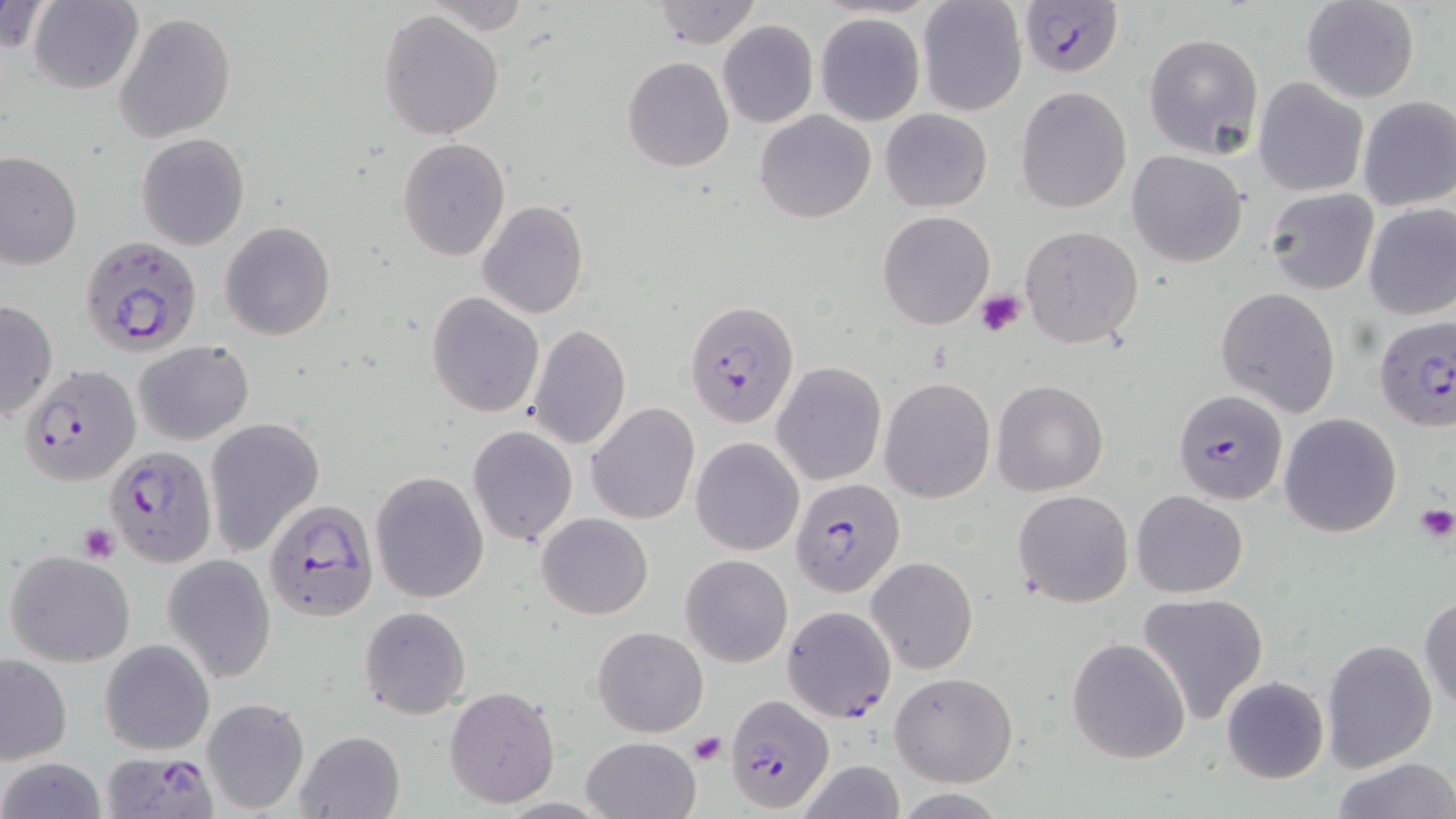
{
  "slide_level_diagnosis": "Plasmodium falciparum",
  "uninfected_red_blood_cell_locations": "approximate bounding boxes as named x1/y1/x2/y2 corners in pixels: (x1=0, y1=0, x2=54, y2=54), (x1=26, y1=0, x2=145, y2=93), (x1=650, y1=0, x2=760, y2=48), (x1=1299, y1=0, x2=1419, y2=102), (x1=916, y1=1, x2=1028, y2=116), (x1=378, y1=9, x2=505, y2=141), (x1=815, y1=11, x2=925, y2=125), (x1=114, y1=12, x2=236, y2=143), (x1=717, y1=20, x2=818, y2=128), (x1=1142, y1=32, x2=1265, y2=159), (x1=622, y1=56, x2=734, y2=172), (x1=1254, y1=78, x2=1369, y2=197), (x1=1015, y1=87, x2=1132, y2=214), (x1=1356, y1=97, x2=1456, y2=211), (x1=880, y1=108, x2=992, y2=212), (x1=755, y1=109, x2=875, y2=223), (x1=136, y1=133, x2=250, y2=250), (x1=397, y1=138, x2=510, y2=261), (x1=1126, y1=150, x2=1250, y2=267), (x1=0, y1=151, x2=82, y2=269), (x1=1263, y1=189, x2=1379, y2=294), (x1=479, y1=201, x2=589, y2=319), (x1=1361, y1=203, x2=1456, y2=321), (x1=877, y1=210, x2=994, y2=330), (x1=220, y1=221, x2=336, y2=341), (x1=1020, y1=226, x2=1142, y2=347), (x1=1216, y1=287, x2=1342, y2=416), (x1=426, y1=292, x2=543, y2=416), (x1=1, y1=299, x2=57, y2=422), (x1=527, y1=324, x2=632, y2=451), (x1=133, y1=340, x2=255, y2=445), (x1=772, y1=363, x2=886, y2=484), (x1=880, y1=377, x2=996, y2=503), (x1=991, y1=379, x2=1108, y2=495), (x1=587, y1=403, x2=700, y2=524), (x1=1278, y1=413, x2=1402, y2=537), (x1=204, y1=417, x2=324, y2=556), (x1=467, y1=425, x2=577, y2=547), (x1=691, y1=437, x2=804, y2=556), (x1=370, y1=471, x2=490, y2=603), (x1=1012, y1=490, x2=1134, y2=608), (x1=1131, y1=490, x2=1248, y2=598), (x1=536, y1=512, x2=654, y2=619), (x1=2, y1=552, x2=134, y2=666), (x1=162, y1=553, x2=277, y2=684), (x1=679, y1=553, x2=794, y2=668), (x1=866, y1=557, x2=977, y2=675), (x1=1136, y1=592, x2=1270, y2=726), (x1=1419, y1=592, x2=1456, y2=716), (x1=359, y1=606, x2=470, y2=719), (x1=592, y1=625, x2=709, y2=737), (x1=1067, y1=637, x2=1191, y2=765), (x1=100, y1=638, x2=215, y2=755), (x1=1320, y1=638, x2=1437, y2=773), (x1=0, y1=654, x2=73, y2=764), (x1=890, y1=672, x2=1018, y2=788), (x1=1222, y1=676, x2=1329, y2=784), (x1=445, y1=687, x2=560, y2=808), (x1=201, y1=697, x2=310, y2=813), (x1=295, y1=730, x2=404, y2=818), (x1=582, y1=735, x2=701, y2=819), (x1=1, y1=758, x2=106, y2=819), (x1=1331, y1=758, x2=1456, y2=818), (x1=796, y1=760, x2=907, y2=819)",
  "image_size": "1456×819 pixels",
  "preparation": "thin blood smear",
  "field_of_view": "one of a larger specimen",
  "magnification": "1000x",
  "stain": "May-Grünwald-Giemsa",
  "plasmodium_falciparum_infected_red_blood_cell_locations": "approximate bounding boxes as named x1/y1/x2/y2 corners in pixels: (x1=1018, y1=0, x2=1125, y2=79), (x1=79, y1=234, x2=202, y2=356), (x1=685, y1=300, x2=800, y2=429), (x1=1374, y1=317, x2=1456, y2=435), (x1=19, y1=362, x2=140, y2=486), (x1=1174, y1=390, x2=1289, y2=506), (x1=104, y1=447, x2=217, y2=566), (x1=791, y1=475, x2=905, y2=596), (x1=263, y1=500, x2=377, y2=622), (x1=781, y1=606, x2=896, y2=722), (x1=725, y1=694, x2=834, y2=813), (x1=103, y1=751, x2=217, y2=815)",
  "modality": "optical microscopy",
  "platelet_locations": "approximate bounding boxes as named x1/y1/x2/y2 corners in pixels: (x1=974, y1=290, x2=1026, y2=338), (x1=1413, y1=503, x2=1456, y2=543), (x1=77, y1=523, x2=120, y2=564), (x1=688, y1=733, x2=727, y2=765)"
}